Report the malaria status.
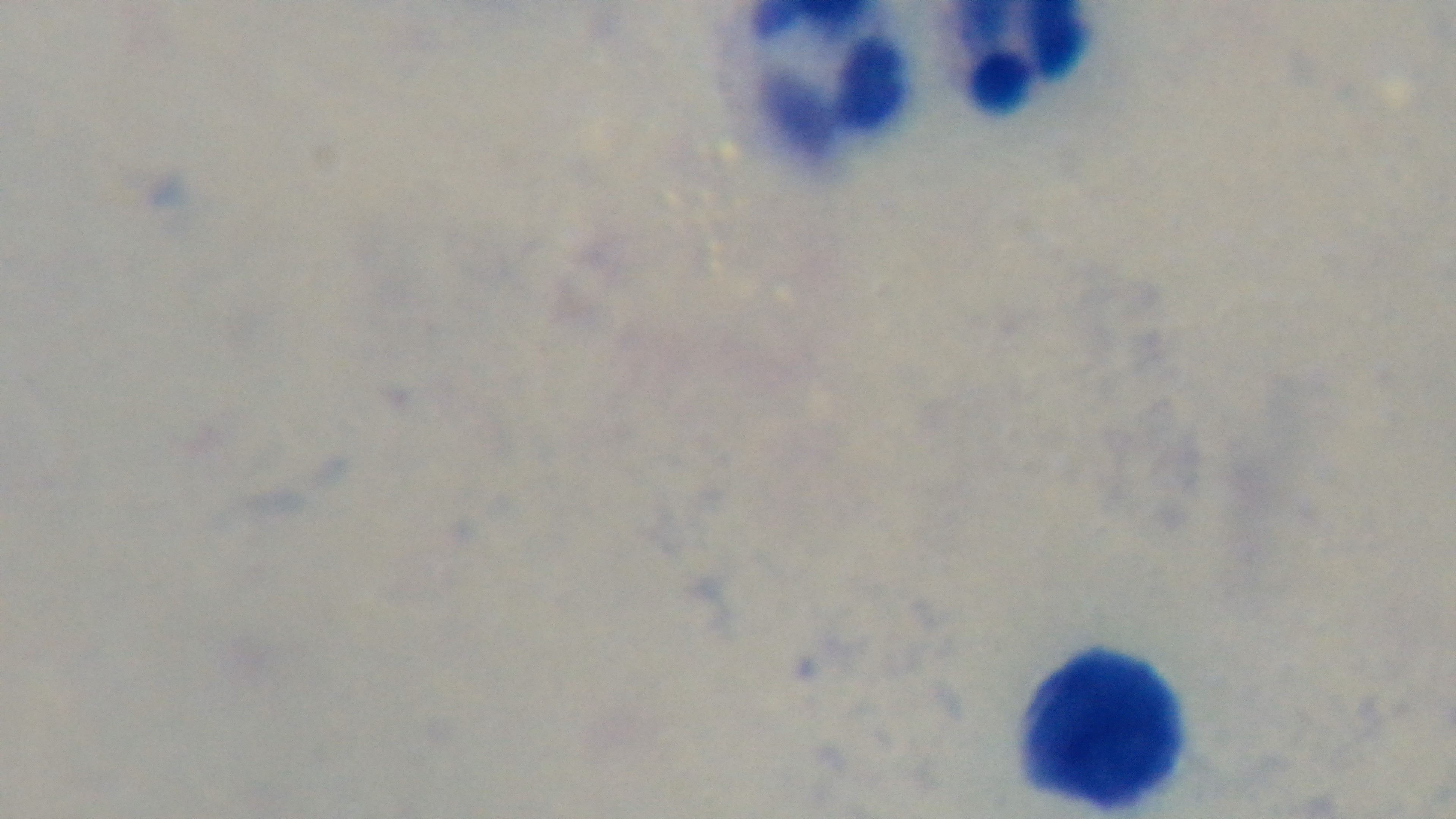
It is uninfected.

Single field of view. Giemsa stain. Preparation: thick smear. 100x oil-immersion objective. Mounted 4K digital camera. Photomicrograph.